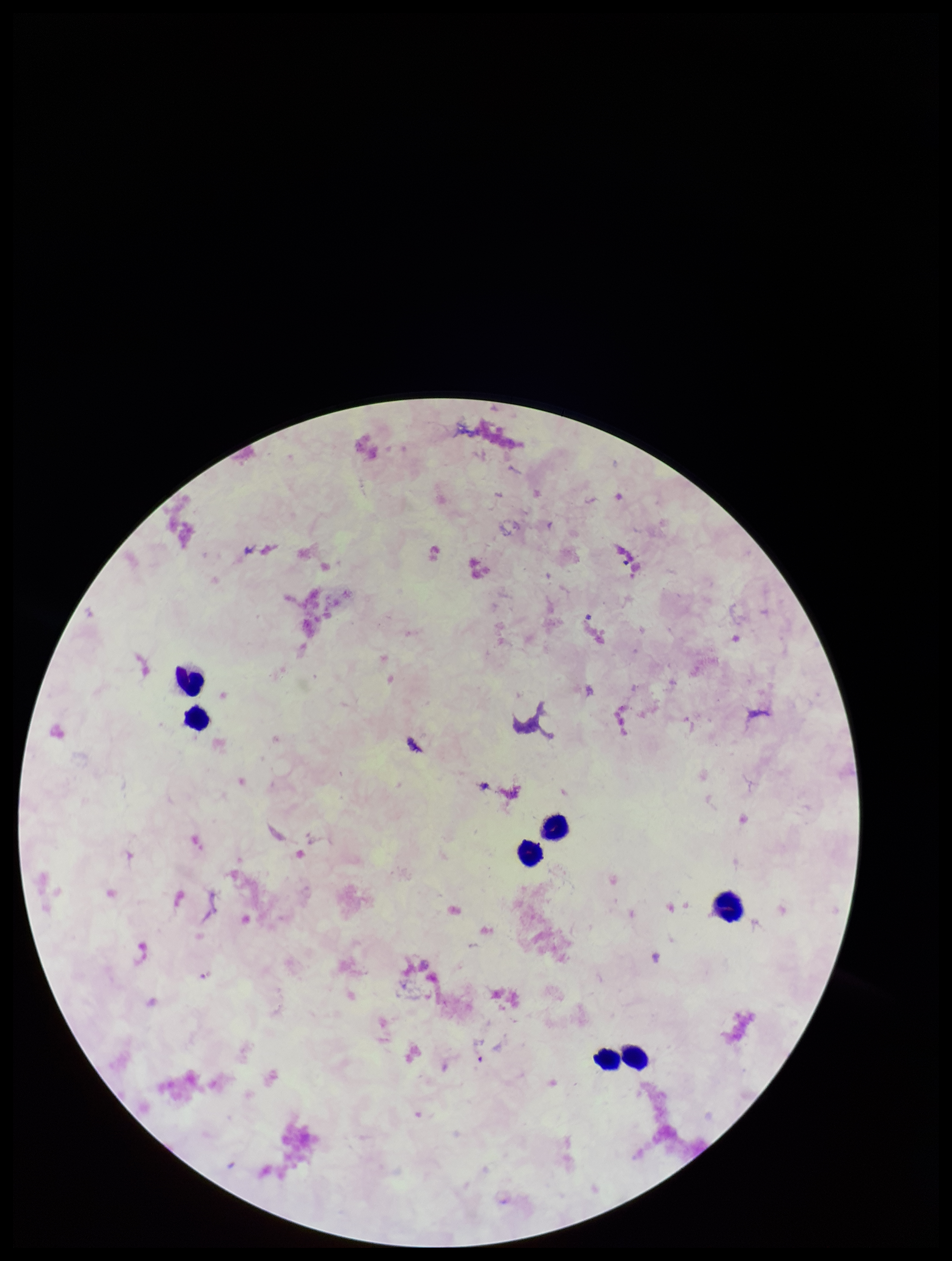

{
  "plasmodium_parasites": "none identified",
  "image_size": "952×1261 pixels",
  "stain": "Giemsa",
  "capture": "smartphone photograph through the microscope eyepiece",
  "patient_malaria_status": "negative",
  "leukocyte_count": 7,
  "field_of_view": "single",
  "preparation": "thick smear",
  "parasite_count": 0
}